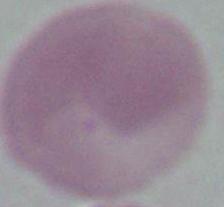

magnification = 1000x
modality = micrograph
identification = red blood cell